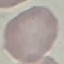
Summary:
  - Malaria status: uninfected
  - Preparation: thin smear
  - Capture: smartphone through the microscope eyepiece
  - Stain: Giemsa
  - Image type: cell patch, automatically extracted from a larger field of view and resized to 64 × 64 pixels